Report the malaria status of this cell.
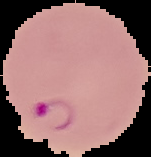
It is parasitized.

Summary:
  - Image type: cell region segmented out of the field of view; surrounding area masked to black
  - Preparation: thin blood film
  - Image size: 151×157 pixels